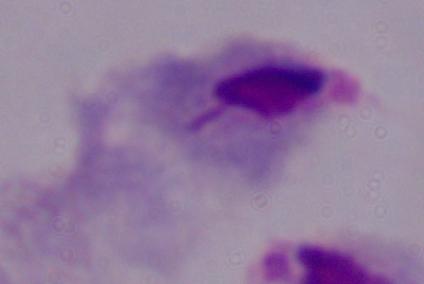
Summary:
  - Magnification: 1000x
  - Modality: photomicrograph
  - Identification: trichomonad